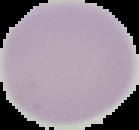 Image is 139×130 pixels. Cell region segmented out of the field of view; the surrounding area is masked to black. Malaria status: uninfected. From a thin blood film.